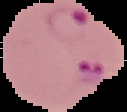

Summary:
  - Image size: 127×112 pixels
  - Image type: segmented cell region on a black background
  - Preparation: thin blood smear
  - Malaria status: parasitized